Classify this cell by malaria status.
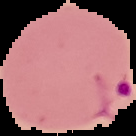

It is parasitized.

Summary:
  - Image type: segmented cell region on a black background
  - Image size: 136×136 pixels
  - Preparation: thin blood film